Identify the cell.
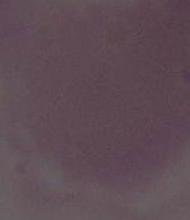
This is an erythrocyte.

Photomicrograph. Captured at 1000x magnification.